Classify this cell by malaria status.
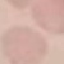

Uninfected.

capture = smartphone through the microscope eyepiece
preparation = thin smear
image type = automatically extracted cell patch, resized to 64 × 64 pixels
stain = Giemsa